Outline each Plasmodium ovale-infected red blood cell.
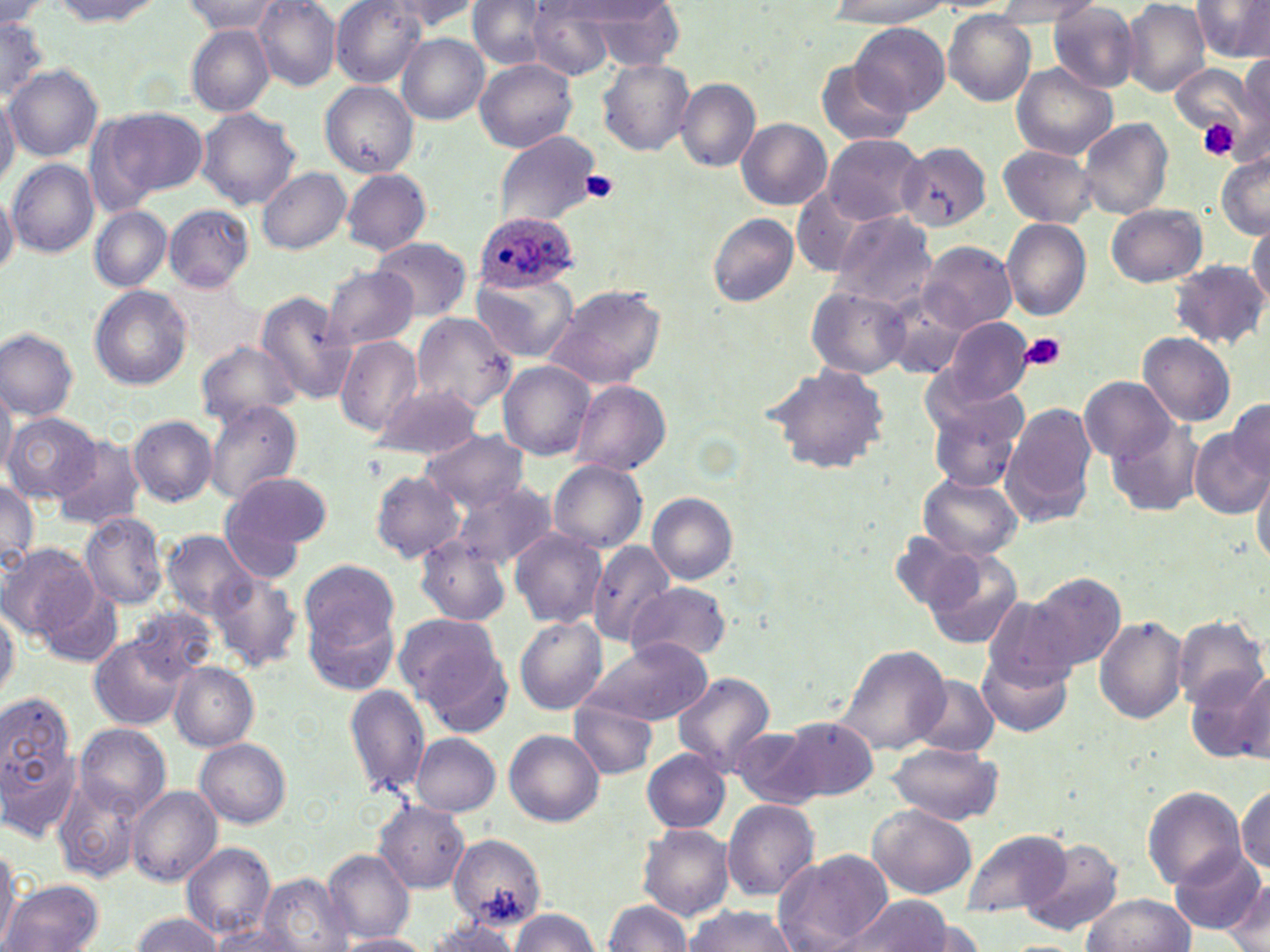

Approximate bounding boxes as named x1/y1/x2/y2 corners in pixels.
Plasmodium ovale-infected red blood cells: (x1=476, y1=211, x2=576, y2=292).

slide-level diagnosis = Plasmodium ovale
modality = optical microscopy
image size = 1270×952 pixels
uninfected red blood cell locations = approximate bounding boxes as named x1/y1/x2/y2 corners in pixels: (x1=251, y1=0, x2=341, y2=90), (x1=330, y1=0, x2=426, y2=87), (x1=378, y1=0, x2=483, y2=33), (x1=989, y1=0, x2=1103, y2=24), (x1=44, y1=1, x2=165, y2=27), (x1=464, y1=1, x2=558, y2=70), (x1=560, y1=1, x2=675, y2=27), (x1=826, y1=1, x2=958, y2=29), (x1=1122, y1=1, x2=1210, y2=98), (x1=1191, y1=1, x2=1269, y2=62), (x1=0, y1=2, x2=54, y2=29), (x1=182, y1=2, x2=285, y2=36), (x1=582, y1=2, x2=685, y2=71), (x1=1048, y1=4, x2=1139, y2=91), (x1=523, y1=5, x2=623, y2=78), (x1=944, y1=12, x2=1036, y2=106), (x1=0, y1=15, x2=53, y2=99), (x1=853, y1=22, x2=948, y2=115), (x1=186, y1=26, x2=275, y2=115), (x1=396, y1=34, x2=488, y2=124), (x1=1238, y1=54, x2=1270, y2=134), (x1=473, y1=58, x2=578, y2=153), (x1=597, y1=58, x2=695, y2=154), (x1=816, y1=60, x2=911, y2=147), (x1=4, y1=63, x2=104, y2=163), (x1=1012, y1=64, x2=1117, y2=161), (x1=1169, y1=65, x2=1257, y2=143), (x1=676, y1=77, x2=761, y2=171), (x1=321, y1=82, x2=417, y2=176), (x1=0, y1=91, x2=19, y2=190), (x1=95, y1=106, x2=209, y2=205), (x1=195, y1=108, x2=301, y2=210), (x1=737, y1=118, x2=832, y2=210), (x1=1077, y1=118, x2=1173, y2=220), (x1=494, y1=130, x2=603, y2=230), (x1=821, y1=133, x2=925, y2=224), (x1=896, y1=143, x2=990, y2=231), (x1=996, y1=144, x2=1099, y2=229), (x1=1216, y1=152, x2=1269, y2=240), (x1=8, y1=158, x2=98, y2=258), (x1=258, y1=167, x2=350, y2=254), (x1=340, y1=168, x2=431, y2=255), (x1=792, y1=187, x2=878, y2=277), (x1=0, y1=188, x2=18, y2=278), (x1=1106, y1=203, x2=1206, y2=286), (x1=164, y1=205, x2=253, y2=292), (x1=90, y1=206, x2=172, y2=291), (x1=831, y1=209, x2=937, y2=309), (x1=707, y1=213, x2=798, y2=307), (x1=1001, y1=219, x2=1093, y2=320), (x1=1247, y1=219, x2=1270, y2=311), (x1=371, y1=237, x2=471, y2=321), (x1=917, y1=242, x2=1016, y2=334), (x1=1169, y1=259, x2=1266, y2=348), (x1=322, y1=266, x2=420, y2=351), (x1=471, y1=273, x2=578, y2=362), (x1=89, y1=285, x2=192, y2=390), (x1=544, y1=285, x2=666, y2=391), (x1=807, y1=286, x2=910, y2=381), (x1=254, y1=292, x2=358, y2=404), (x1=886, y1=293, x2=969, y2=380), (x1=411, y1=311, x2=519, y2=417), (x1=941, y1=316, x2=1034, y2=405), (x1=0, y1=327, x2=80, y2=418), (x1=1137, y1=331, x2=1236, y2=427), (x1=334, y1=335, x2=424, y2=437), (x1=196, y1=341, x2=298, y2=425), (x1=498, y1=360, x2=595, y2=460), (x1=764, y1=364, x2=890, y2=473), (x1=922, y1=365, x2=1022, y2=456), (x1=1077, y1=377, x2=1179, y2=462), (x1=0, y1=380, x2=16, y2=481), (x1=571, y1=380, x2=671, y2=476), (x1=370, y1=384, x2=484, y2=460), (x1=1229, y1=397, x2=1270, y2=478), (x1=204, y1=399, x2=304, y2=505), (x1=930, y1=399, x2=1024, y2=492), (x1=1003, y1=402, x2=1099, y2=523), (x1=3, y1=411, x2=102, y2=501), (x1=128, y1=415, x2=217, y2=506), (x1=1106, y1=417, x2=1204, y2=517), (x1=420, y1=428, x2=530, y2=512), (x1=1191, y1=428, x2=1268, y2=518), (x1=53, y1=438, x2=147, y2=530), (x1=548, y1=460, x2=647, y2=554), (x1=1252, y1=465, x2=1270, y2=569), (x1=368, y1=470, x2=467, y2=563), (x1=219, y1=471, x2=332, y2=575), (x1=917, y1=471, x2=1024, y2=562), (x1=451, y1=479, x2=556, y2=572), (x1=0, y1=480, x2=39, y2=572), (x1=647, y1=493, x2=738, y2=584), (x1=79, y1=510, x2=170, y2=610), (x1=509, y1=528, x2=608, y2=628), (x1=159, y1=531, x2=258, y2=622), (x1=891, y1=533, x2=985, y2=614), (x1=414, y1=536, x2=511, y2=626), (x1=587, y1=538, x2=673, y2=648), (x1=2, y1=544, x2=99, y2=641), (x1=921, y1=545, x2=1025, y2=649), (x1=299, y1=561, x2=399, y2=651), (x1=208, y1=570, x2=301, y2=671), (x1=1024, y1=571, x2=1126, y2=674), (x1=628, y1=582, x2=731, y2=665), (x1=40, y1=585, x2=123, y2=667), (x1=301, y1=596, x2=402, y2=697), (x1=0, y1=600, x2=17, y2=704), (x1=125, y1=606, x2=221, y2=687), (x1=393, y1=611, x2=504, y2=712), (x1=1094, y1=614, x2=1189, y2=724), (x1=514, y1=616, x2=607, y2=716), (x1=1173, y1=616, x2=1267, y2=713), (x1=89, y1=635, x2=193, y2=731), (x1=583, y1=637, x2=714, y2=726), (x1=835, y1=645, x2=954, y2=756), (x1=981, y1=647, x2=1073, y2=736), (x1=169, y1=663, x2=259, y2=749), (x1=1226, y1=668, x2=1269, y2=764), (x1=672, y1=671, x2=773, y2=772), (x1=912, y1=675, x2=998, y2=758), (x1=345, y1=682, x2=432, y2=796), (x1=0, y1=696, x2=82, y2=838), (x1=574, y1=699, x2=657, y2=779), (x1=783, y1=718, x2=878, y2=802), (x1=75, y1=724, x2=170, y2=817), (x1=728, y1=726, x2=827, y2=810), (x1=504, y1=730, x2=604, y2=826), (x1=410, y1=733, x2=500, y2=816), (x1=195, y1=738, x2=290, y2=828), (x1=886, y1=741, x2=1002, y2=825), (x1=642, y1=750, x2=731, y2=834), (x1=55, y1=781, x2=141, y2=882), (x1=1234, y1=783, x2=1268, y2=874), (x1=126, y1=786, x2=222, y2=885), (x1=1143, y1=787, x2=1246, y2=887), (x1=723, y1=799, x2=820, y2=899), (x1=377, y1=801, x2=471, y2=892), (x1=867, y1=805, x2=976, y2=898), (x1=638, y1=824, x2=733, y2=920), (x1=960, y1=829, x2=1069, y2=917), (x1=447, y1=833, x2=545, y2=928), (x1=0, y1=837, x2=19, y2=951), (x1=1017, y1=838, x2=1125, y2=937), (x1=182, y1=842, x2=276, y2=939), (x1=1169, y1=846, x2=1266, y2=936), (x1=774, y1=848, x2=893, y2=949), (x1=322, y1=849, x2=415, y2=941), (x1=258, y1=872, x2=355, y2=952), (x1=1225, y1=875, x2=1270, y2=951), (x1=3, y1=880, x2=104, y2=951), (x1=1081, y1=893, x2=1195, y2=952), (x1=845, y1=895, x2=955, y2=952), (x1=602, y1=900, x2=694, y2=950), (x1=682, y1=905, x2=798, y2=951), (x1=509, y1=908, x2=600, y2=952), (x1=128, y1=914, x2=224, y2=951), (x1=418, y1=921, x2=523, y2=951), (x1=206, y1=923, x2=306, y2=952), (x1=338, y1=933, x2=429, y2=952)
field of view = single
preparation = thin blood smear
platelet locations = approximate bounding boxes as named x1/y1/x2/y2 corners in pixels: (x1=1197, y1=119, x2=1239, y2=161), (x1=580, y1=170, x2=619, y2=201), (x1=1019, y1=333, x2=1068, y2=372)
magnification = 1000x
stain = May-Grünwald-Giemsa